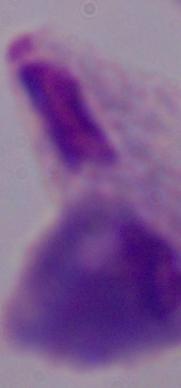
{
  "identification": "trichomonad",
  "magnification": "1000x",
  "modality": "micrograph"
}